Look for parasitized red blood cells.
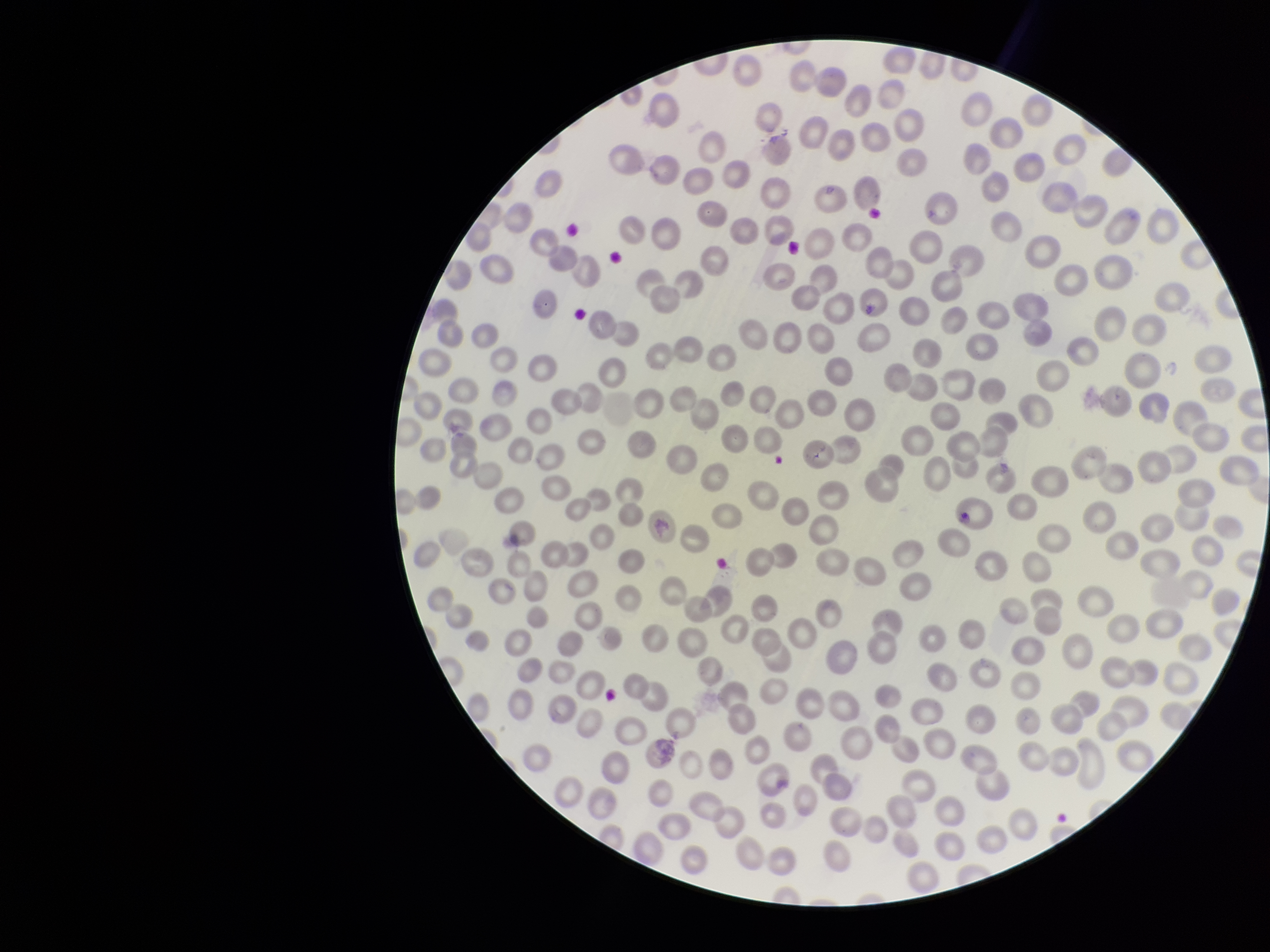

None identified.

Summary:
  - Red blood cell count: 277
  - Field of view: single
  - Stain: Giemsa
  - Preparation: thin
  - Capture: smartphone photograph through the microscope eyepiece
  - Species reported for this patient: Plasmodium vivax
  - Parasitized red blood cell count: 0
  - Image size: 1270×952 pixels
  - Patient malaria status: infected